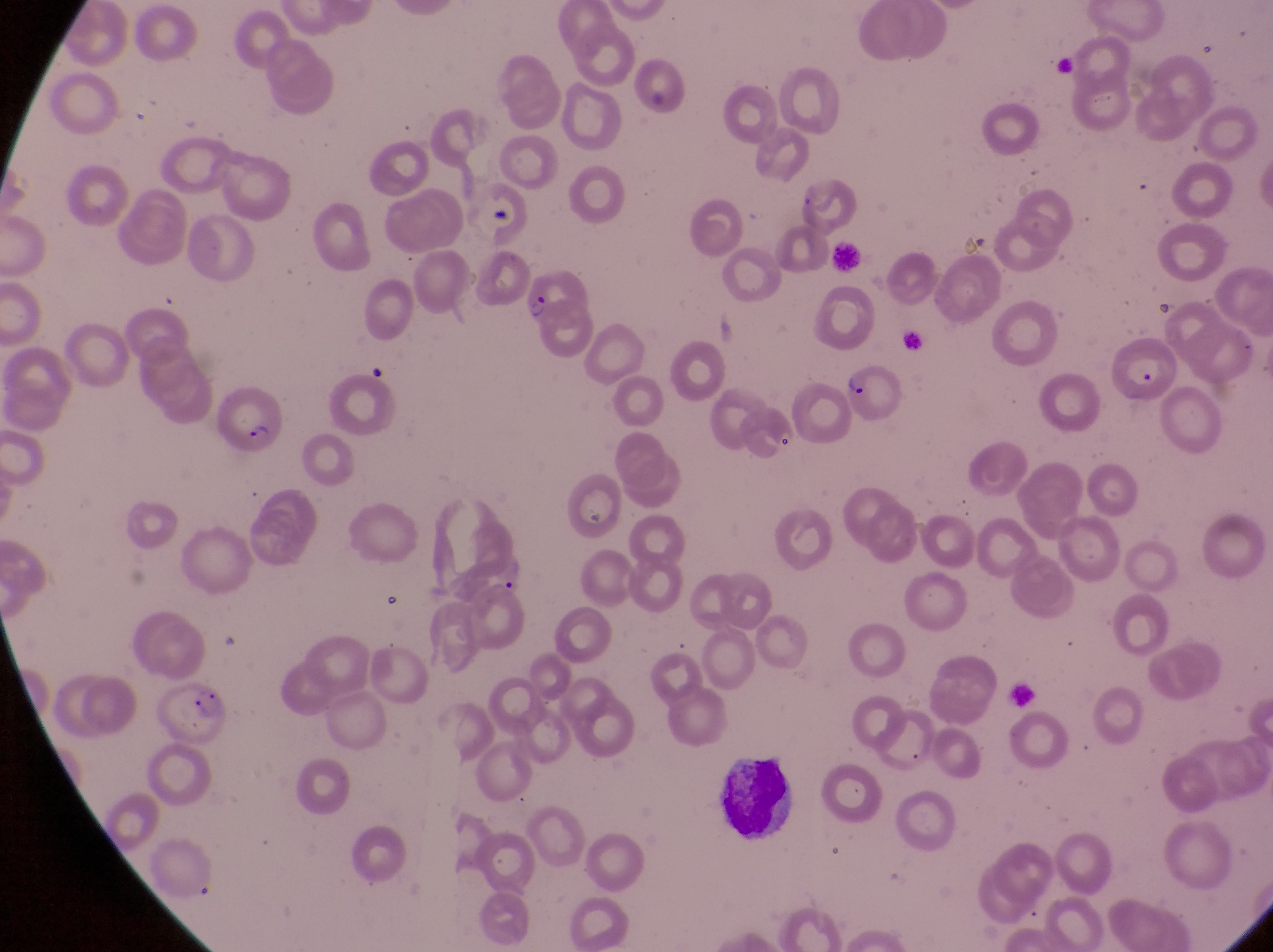
magnification = 1000x
artifact (platelet-like body, stain precipitate, or debris) locations = approximate bounding boxes as left top right bottom in pixels: 581 500 618 535
field of view = single
capture = smartphone photograph through the eyepiece of an Olympus CX-23 microscope
preparation = thin blood smear
image size = 1273×952 pixels
leukocyte locations = approximate bounding boxes as left top right bottom in pixels: 715 742 807 847
country = Uganda
parasitised red blood cell locations = approximate bounding boxes as left top right bottom in pixels: 526 265 593 333; 1115 330 1182 402; 841 357 906 424; 215 375 278 452; 731 394 801 464; 157 674 232 746